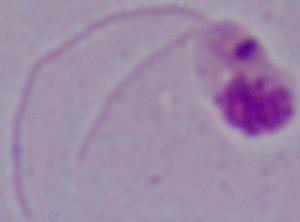 A Leishmania parasite is seen. Photomicrograph. 1000x magnification.